Identify the cell.
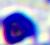

A leukocyte.

modality = micrograph
magnification = 400x